Assess this cell for malaria.
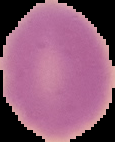
Uninfected.

Summary:
  - Image type: segmented cell region on a black background
  - Preparation: thin blood smear
  - Image size: 115×142 pixels